Assess this cell for malaria.
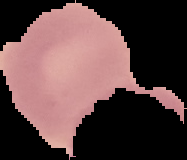

Uninfected.

From a thin blood film. Image is 187×160 pixels. Cell region segmented out of the field of view; the surrounding area is masked to black.